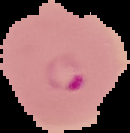
Image is 130×133 pixels. Malaria status: parasitized. The area outside the segmented cell region is set to black. From a thin blood film.